Evaluate for Plasmodium parasites.
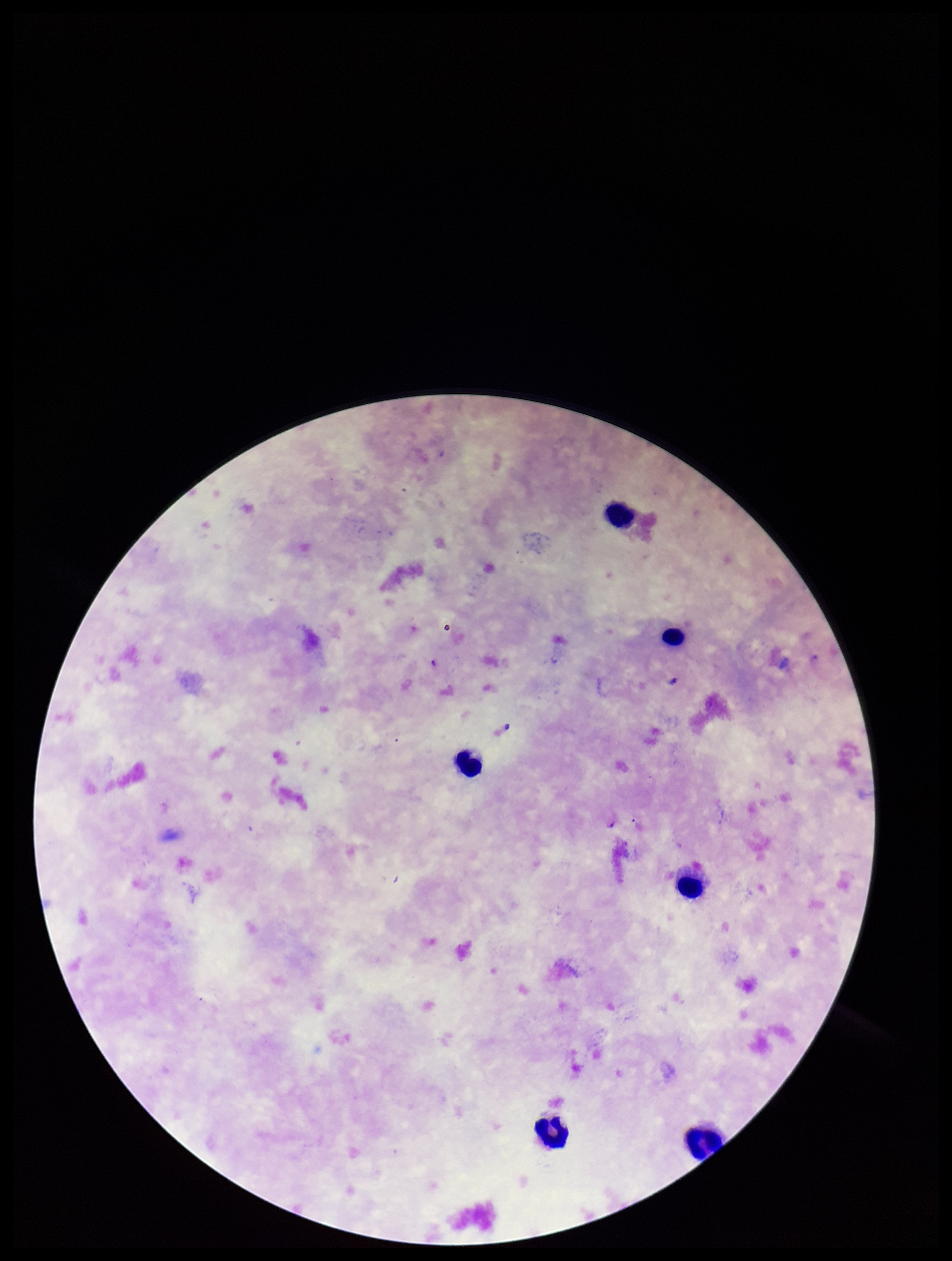
None detected.

Single field of view. Stained with Giemsa. Species reported for this patient: Plasmodium falciparum. Patient malaria status: positive. Image is 952×1261 pixels. Leukocyte count: 6. Parasite count: 0. Smartphone photograph taken through the eyepiece of a microscope. Preparation: thick.